Assess the morphology of the erythrocytes.
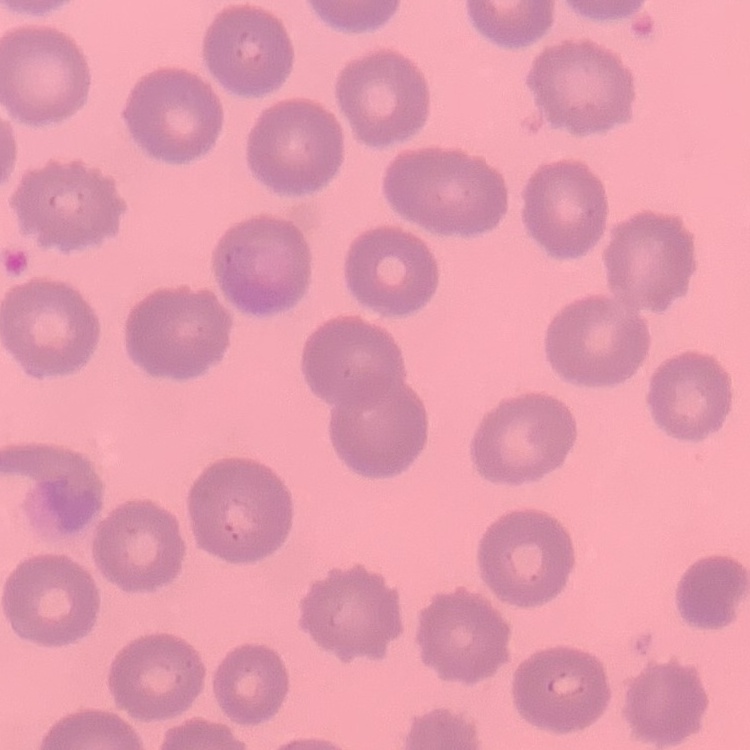
They show no rouleaux formation.

Field's or Giemsa stain. Thin blood film. Square crop of a larger photomicrograph.